Name the blood parasite species.
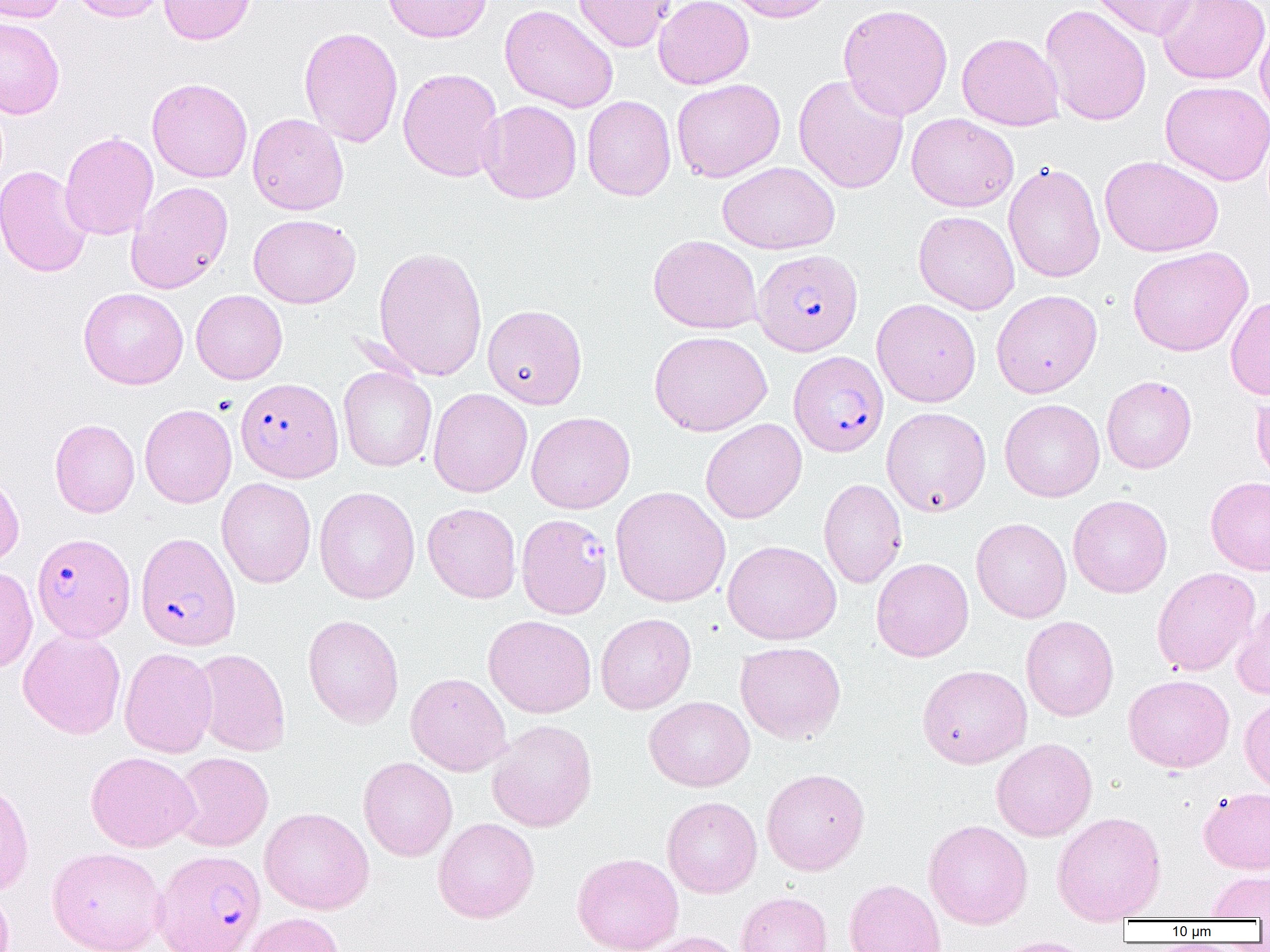

Plasmodium falciparum.

Approximate bounding boxes as (x1, y1, x2, y2) in pixels. Plasmodium falciparum-infected red blood cell locations (subset): (753, 249, 863, 355), (789, 351, 889, 457), (235, 378, 343, 482), (135, 532, 241, 651), (32, 533, 135, 642), (153, 849, 266, 952). Uninfected red blood cell locations (subset): (0, 0, 67, 23), (70, 0, 170, 23), (159, 0, 255, 45), (383, 0, 492, 43), (574, 0, 675, 52), (654, 0, 754, 89), (724, 0, 837, 23), (1091, 0, 1201, 40), (1156, 0, 1269, 84), (838, 3, 953, 121), (499, 4, 618, 113), (1039, 4, 1152, 127), (0, 17, 65, 119), (1255, 20, 1270, 126), (299, 26, 403, 147), (957, 32, 1064, 131), (398, 67, 504, 182), (793, 73, 909, 194), (147, 78, 253, 183), (672, 78, 785, 182), (1160, 81, 1270, 185), (582, 95, 676, 202), (477, 100, 582, 204), (248, 113, 349, 215), (906, 113, 1019, 212), (60, 131, 158, 240), (1099, 155, 1223, 257), (718, 161, 839, 254), (1004, 162, 1105, 283), (0, 165, 93, 278), (126, 181, 234, 294), (913, 211, 1019, 315), (249, 214, 360, 308), (648, 234, 762, 334), (373, 246, 488, 381), (1127, 246, 1253, 356), (78, 287, 188, 389), (191, 289, 287, 384), (991, 289, 1102, 398), (1226, 295, 1270, 400), (872, 298, 981, 407), (482, 304, 587, 409), (649, 330, 772, 436), (338, 366, 437, 472), (1102, 375, 1197, 473), (428, 388, 532, 498), (1251, 391, 1270, 491), (999, 398, 1105, 502), (139, 404, 236, 508), (881, 407, 991, 516), (526, 411, 635, 513), (700, 418, 806, 523), (50, 419, 140, 517), (0, 469, 24, 567), (1205, 476, 1270, 575), (216, 477, 316, 588), (819, 478, 907, 589), (610, 486, 731, 607), (314, 487, 420, 604), (1068, 494, 1172, 598), (422, 503, 522, 603), (971, 517, 1072, 623), (722, 540, 841, 644), (871, 557, 974, 662), (0, 566, 38, 673), (1152, 567, 1260, 676), (1231, 598, 1270, 699), (595, 613, 696, 714), (303, 615, 404, 728), (483, 615, 596, 717), (1021, 615, 1119, 721), (18, 628, 126, 739), (734, 641, 846, 744), (119, 647, 218, 758), (192, 648, 291, 756), (917, 664, 1032, 768), (405, 672, 512, 776), (1123, 674, 1234, 773), (1239, 695, 1270, 795), (644, 696, 755, 791), (487, 720, 598, 832), (990, 738, 1097, 841), (86, 751, 200, 852), (172, 752, 274, 852), (358, 757, 457, 861), (761, 768, 870, 875), (0, 776, 34, 896), (1198, 786, 1270, 874), (662, 796, 762, 898), (259, 807, 374, 914), (1051, 811, 1167, 924), (432, 817, 539, 923), (923, 819, 1033, 929), (47, 846, 167, 952), (572, 852, 684, 952), (1207, 871, 1270, 919), (844, 878, 946, 952), (0, 883, 14, 952), (736, 892, 833, 952), (242, 911, 345, 952), (639, 931, 749, 952), (991, 937, 1096, 952). Light microscopy. One field of a larger specimen. 1000x magnification. Thin blood film. Image is 1270×952 pixels.